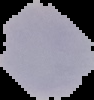

image_size: 94×100 pixels
image_type: segmented cell region with the area outside set to black
preparation: thin blood film
result: no malaria parasites seen